Describe the morphology of the erythrocytes.
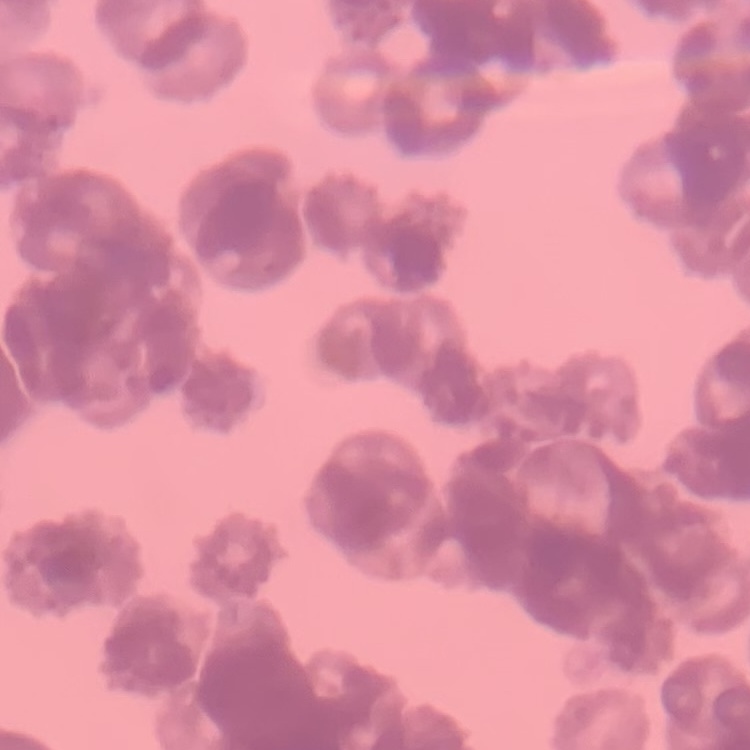
They show rouleaux formation.

image type = square crop of a larger photomicrograph
preparation = thin blood film
stain = Field's or Giemsa